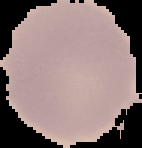
Summary:
  - Image type: cell region segmented out of the field of view; surrounding area masked to black
  - Preparation: thin blood smear
  - Image size: 142×148 pixels
  - Result: negative for Plasmodium parasites